Assess this cell for malaria.
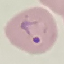

Parasitized.

Summary:
  - Stain: Giemsa
  - Capture: smartphone through the microscope eyepiece
  - Image type: automatically extracted cell patch, resized to 64 × 64 pixels
  - Preparation: thin blood smear